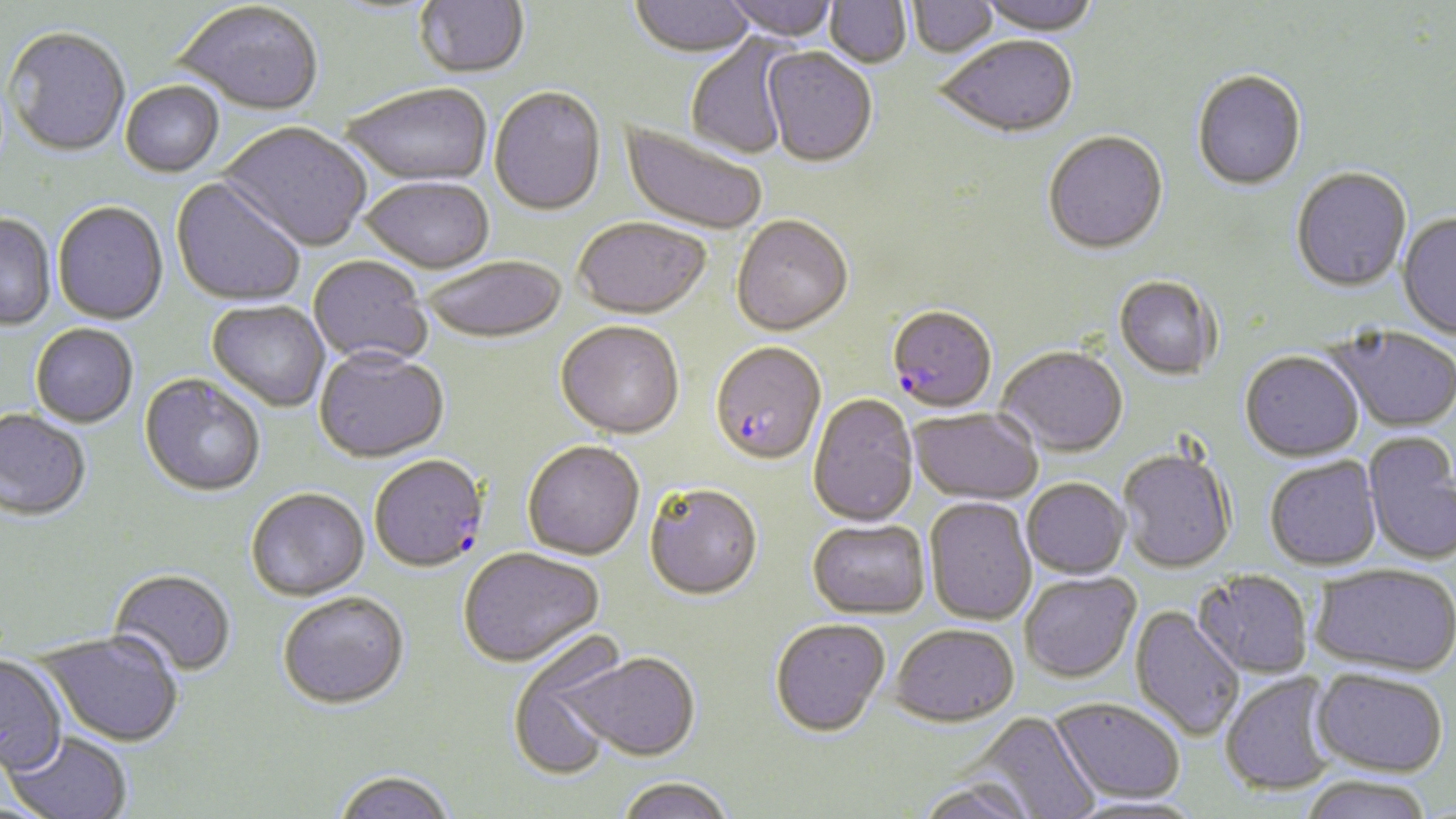

Summary:
  - Coordinate format: approximate bounding boxes as named x1/y1/x2/y2 corners in pixels
  - Plasmodium falciparum-infected red blood cell locations: (x1=890, y1=310, x2=997, y2=418), (x1=710, y1=343, x2=827, y2=467), (x1=369, y1=456, x2=489, y2=575)
  - Uninfected red blood cell locations: (x1=414, y1=0, x2=530, y2=80), (x1=629, y1=0, x2=756, y2=61), (x1=720, y1=0, x2=841, y2=42), (x1=825, y1=0, x2=912, y2=69), (x1=908, y1=0, x2=999, y2=60), (x1=975, y1=0, x2=1100, y2=37), (x1=174, y1=5, x2=324, y2=119), (x1=3, y1=29, x2=131, y2=159), (x1=685, y1=35, x2=795, y2=160), (x1=936, y1=38, x2=1078, y2=140), (x1=762, y1=49, x2=877, y2=169), (x1=1192, y1=72, x2=1307, y2=192), (x1=120, y1=83, x2=225, y2=179), (x1=342, y1=86, x2=493, y2=188), (x1=489, y1=88, x2=606, y2=218), (x1=617, y1=120, x2=768, y2=237), (x1=218, y1=123, x2=372, y2=253), (x1=1043, y1=133, x2=1169, y2=257), (x1=1291, y1=169, x2=1413, y2=293), (x1=170, y1=179, x2=306, y2=308), (x1=359, y1=179, x2=495, y2=275), (x1=52, y1=203, x2=168, y2=327), (x1=1397, y1=213, x2=1456, y2=341), (x1=0, y1=215, x2=56, y2=331), (x1=731, y1=217, x2=854, y2=338), (x1=574, y1=219, x2=711, y2=321), (x1=308, y1=257, x2=433, y2=368), (x1=422, y1=258, x2=568, y2=346), (x1=1114, y1=277, x2=1219, y2=381), (x1=206, y1=301, x2=330, y2=412), (x1=555, y1=322, x2=684, y2=441), (x1=30, y1=325, x2=138, y2=428), (x1=1326, y1=326, x2=1456, y2=434), (x1=995, y1=346, x2=1128, y2=458), (x1=314, y1=350, x2=449, y2=465), (x1=1240, y1=353, x2=1364, y2=463), (x1=139, y1=375, x2=265, y2=498), (x1=808, y1=394, x2=919, y2=528), (x1=909, y1=408, x2=1043, y2=505), (x1=0, y1=410, x2=91, y2=522), (x1=1363, y1=433, x2=1456, y2=566), (x1=522, y1=442, x2=644, y2=562), (x1=1118, y1=447, x2=1236, y2=574), (x1=1265, y1=457, x2=1383, y2=571), (x1=1021, y1=479, x2=1129, y2=579), (x1=644, y1=484, x2=762, y2=602), (x1=246, y1=490, x2=370, y2=602), (x1=924, y1=498, x2=1038, y2=626), (x1=807, y1=519, x2=930, y2=620), (x1=458, y1=549, x2=605, y2=670), (x1=1309, y1=563, x2=1455, y2=675), (x1=108, y1=570, x2=237, y2=679), (x1=1193, y1=571, x2=1313, y2=679), (x1=1019, y1=572, x2=1141, y2=684), (x1=277, y1=594, x2=409, y2=712), (x1=1130, y1=606, x2=1245, y2=741), (x1=770, y1=619, x2=891, y2=739), (x1=890, y1=626, x2=1019, y2=730), (x1=35, y1=631, x2=184, y2=748), (x1=508, y1=640, x2=626, y2=781), (x1=561, y1=652, x2=701, y2=763), (x1=0, y1=656, x2=68, y2=775), (x1=1312, y1=667, x2=1449, y2=776), (x1=1219, y1=672, x2=1340, y2=796), (x1=1050, y1=698, x2=1186, y2=803), (x1=971, y1=712, x2=1101, y2=819), (x1=3, y1=730, x2=134, y2=819), (x1=332, y1=771, x2=457, y2=819), (x1=1297, y1=776, x2=1436, y2=819), (x1=616, y1=778, x2=735, y2=819), (x1=915, y1=781, x2=1039, y2=819)
  - Slide-level diagnosis: Plasmodium falciparum
  - Stain: May-Grünwald-Giemsa
  - Preparation: thin blood film
  - Modality: light microscopy
  - Field of view: single
  - Magnification: 1000x
  - Image size: 1456×819 pixels